Classify this cell by malaria status.
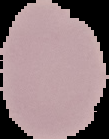

It is uninfected.

Cell region segmented out of the field of view; the surrounding area is masked to black. From a thin blood smear. Image is 109×139 pixels.